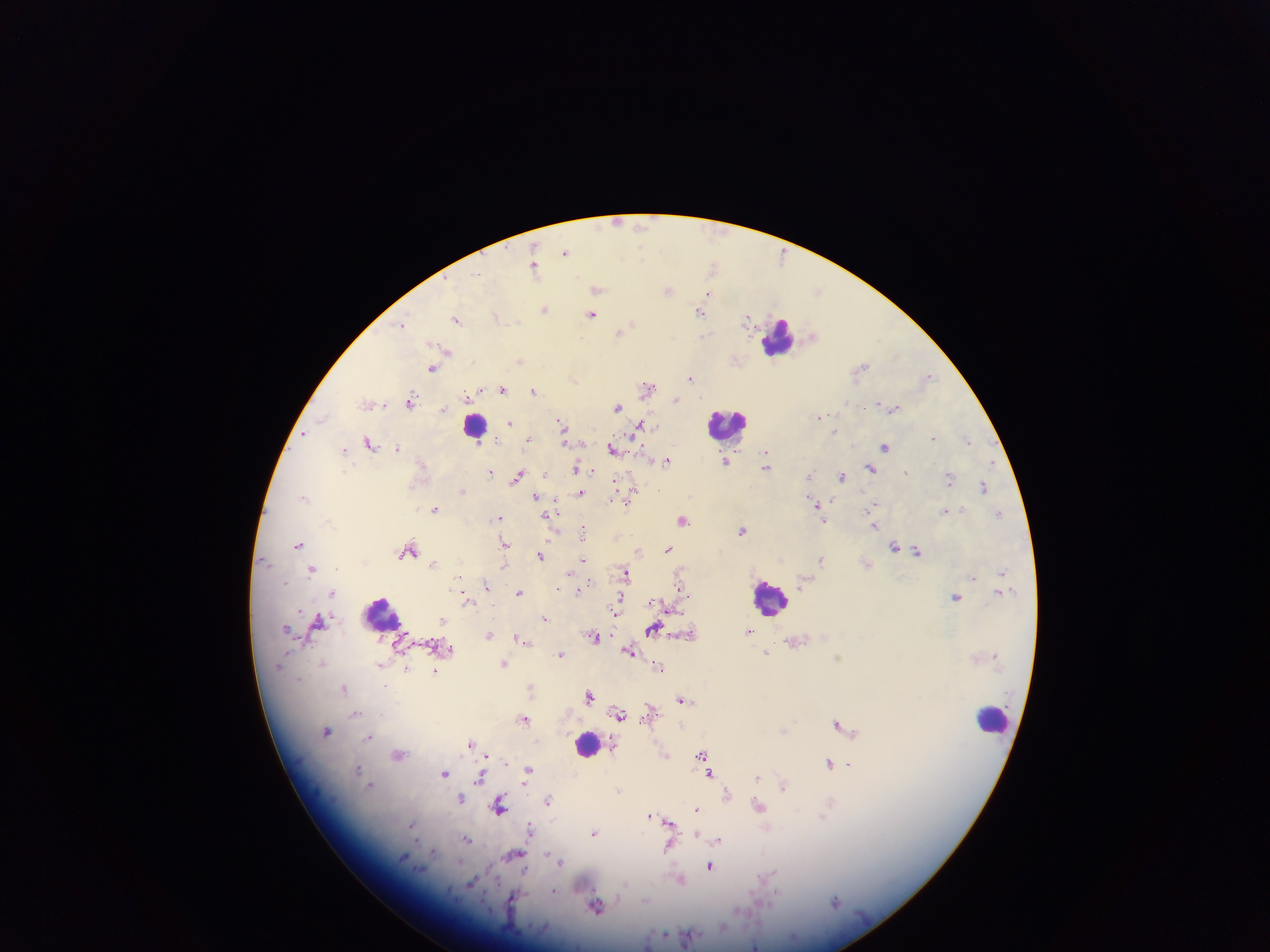
Approximate centers as (x, y) in pixels. Leukocyte locations: (779, 336), (474, 424), (728, 425), (768, 599), (383, 614), (992, 717), (587, 744). Plasmodium parasite locations: (642, 227), (565, 251), (714, 265), (534, 267), (479, 274), (598, 289), (667, 289), (818, 291), (709, 294), (545, 309), (700, 312), (592, 314), (496, 316), (747, 318), (457, 319), (403, 325), (620, 332), (703, 336), (813, 336), (447, 351), (520, 360), (861, 367), (432, 368), (928, 376), (574, 378), (691, 378), (648, 386), (502, 388), (479, 391), (534, 391), (675, 399), (411, 401), (368, 404), (617, 407), (893, 408), (444, 409), (820, 416), (323, 418), (509, 422), (561, 423), (638, 426), (835, 430), (304, 435), (565, 436), (934, 437), (528, 439), (968, 440), (370, 443), (398, 448), (885, 448), (614, 449), (343, 450), (766, 453), (667, 460), (726, 462), (766, 467), (578, 468), (871, 468), (490, 471), (809, 475), (517, 476), (842, 476), (949, 478), (631, 487), (983, 487), (462, 491), (532, 493), (580, 493), (303, 497), (536, 497), (627, 503), (873, 505), (817, 507), (435, 508), (960, 508), (945, 511), (870, 512), (998, 514), (499, 517), (823, 519), (683, 520), (873, 526), (742, 530), (582, 532), (504, 543), (298, 544), (895, 546), (668, 548), (410, 550), (918, 551), (639, 552), (541, 555), (584, 559), (820, 560), (265, 561), (435, 563), (311, 569), (569, 572), (1002, 572), (625, 573), (974, 576), (804, 581), (486, 585), (580, 589), (519, 592), (333, 593), (955, 598), (467, 599), (620, 599), (656, 603), (617, 608), (545, 618), (320, 622), (443, 622), (286, 629), (653, 630), (749, 631), (489, 635), (517, 636), (593, 636), (629, 651), (767, 652), (561, 654), (322, 662), (504, 663), (380, 664), (659, 666), (406, 668), (435, 672), (530, 687), (344, 688), (590, 695), (682, 700), (650, 711), (355, 713), (620, 714), (524, 719), (839, 725), (785, 731), (326, 732), (370, 737), (471, 743), (399, 755), (702, 755), (485, 756), (666, 756), (705, 762), (829, 763), (849, 764), (358, 769), (528, 771), (444, 774), (711, 774), (480, 777), (757, 777), (370, 785), (784, 785), (619, 789), (727, 794), (461, 798), (549, 799), (500, 805), (759, 806), (696, 809), (827, 809), (651, 816), (656, 818), (669, 823), (411, 827), (531, 828), (594, 833), (696, 834), (466, 839), (718, 840), (668, 848), (547, 854), (514, 856), (561, 862), (710, 866), (525, 870), (768, 876), (680, 879), (471, 883), (555, 891), (513, 899), (835, 901), (597, 906), (755, 946). Thick blood film. One field of view. Collected in Ghana. Image is 1270×952 pixels. Mobile-phone photograph taken through the microscope.